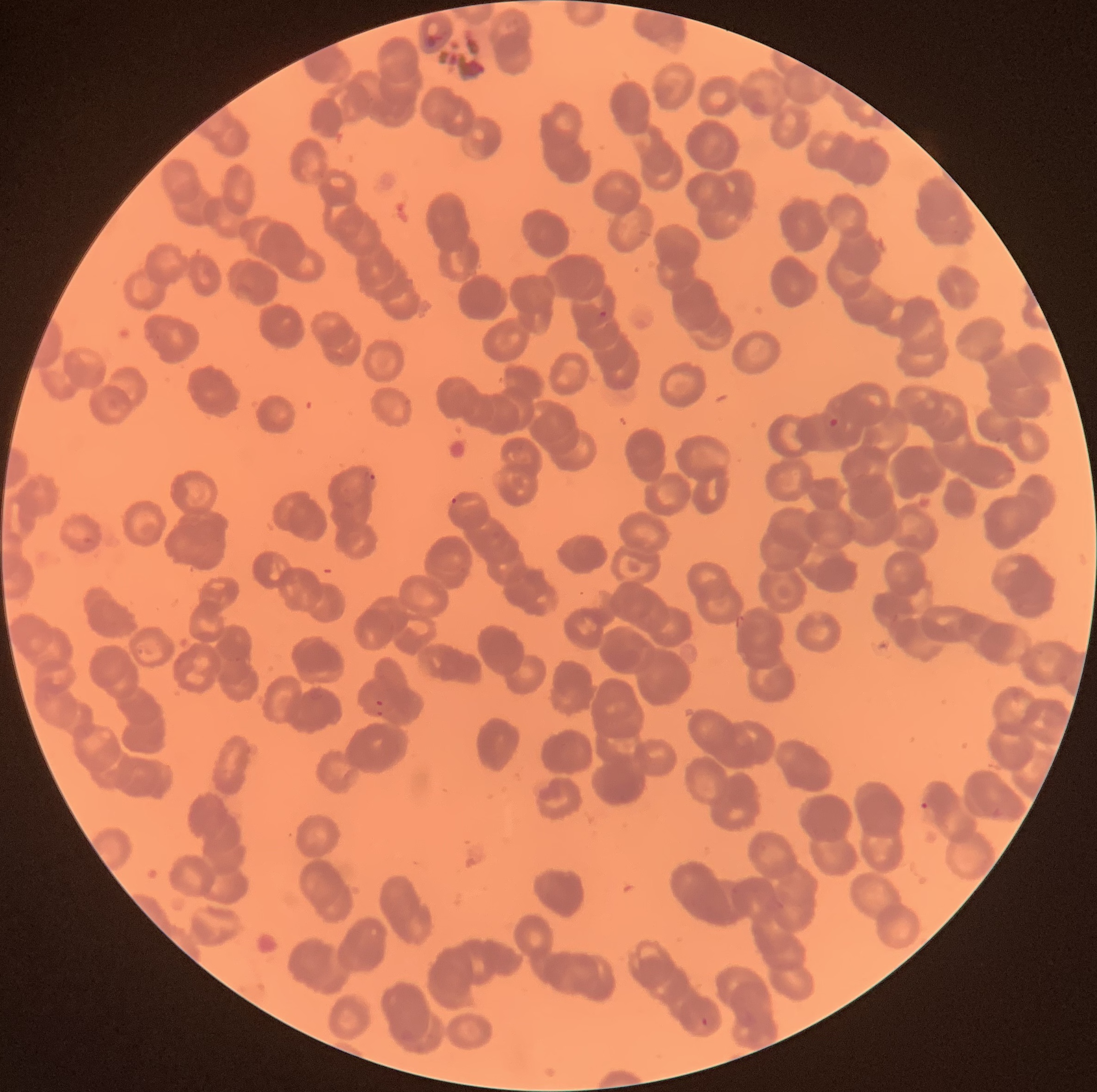

Summary:
  - Coordinate format: approximate bounding boxes as (x1,y1)-(x2,y2) corner pairs in pixels
  - Plasmodium parasite locations: (426,35)-(437,49), (366,97)-(374,104), (599,310)-(607,319), (828,417)-(846,448), (1003,467)-(1017,473), (366,470)-(377,485), (451,497)-(458,505), (82,536)-(91,543), (305,689)-(324,701), (369,699)-(393,718), (920,802)-(937,824), (993,808)-(1003,819), (775,900)-(785,909), (701,1017)-(708,1025)
  - Plasmodium parasites too small for a box (approximate centers as (x,y) in pixels): (999,440)
  - Image size: 1097×1092 pixels
  - Modality: optical microscopy
  - Preparation: thin blood smear
  - Red blood cell morphology: rouleaux formation